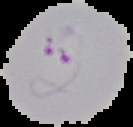
The area outside the segmented cell region is set to black. From a thin blood smear. Image is 133×127 pixels. Result: Plasmodium parasites detected.